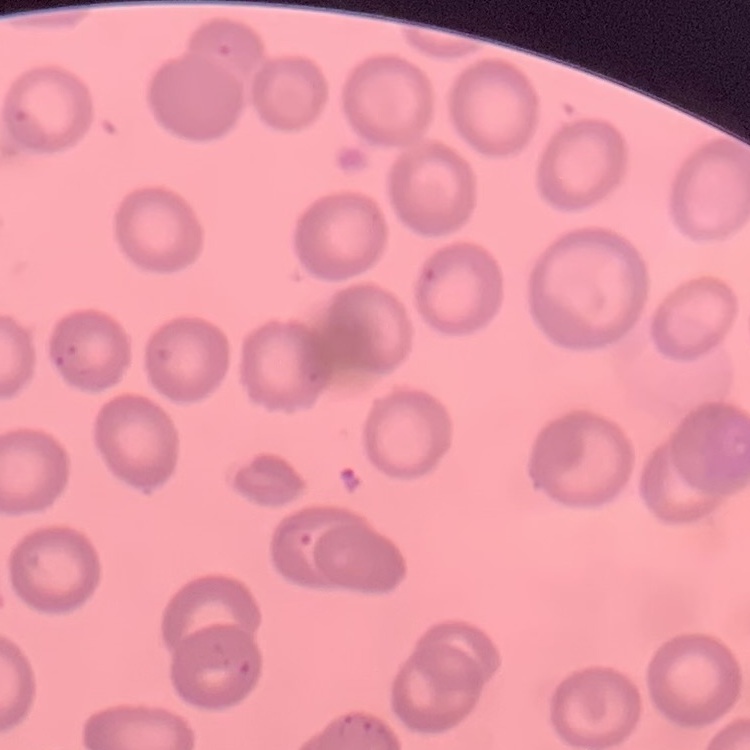

Summary:
  - Red blood cell morphology: no rouleaux formation
  - Image type: square crop of a larger photomicrograph
  - Stain: Field's or Giemsa
  - Preparation: thin blood smear